Assess the morphology of the erythrocytes.
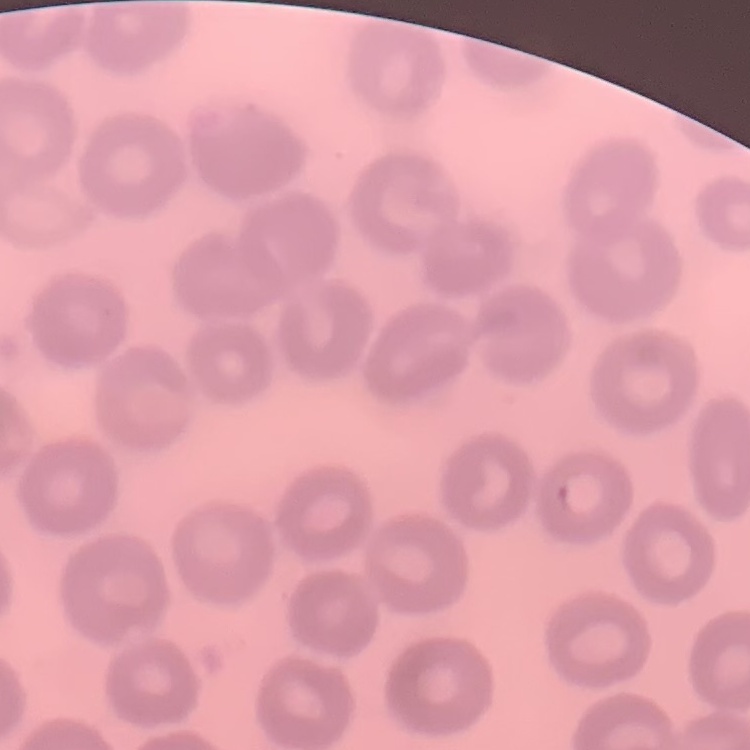

They show no rouleaux formation.

preparation = thin blood film
image type = one tile cut from a larger photomicrograph
stain = Field's or Giemsa